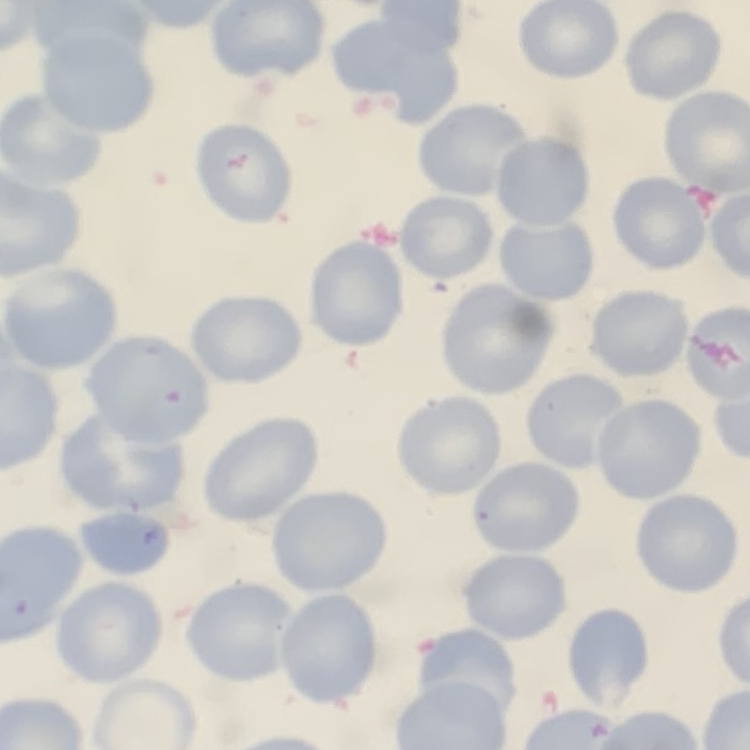
red_blood_cell_morphology: no rouleaux formation
stain: Field's or Giemsa
preparation: thin blood smear
image_type: one tile cut from a larger photomicrograph